State the blood parasite species.
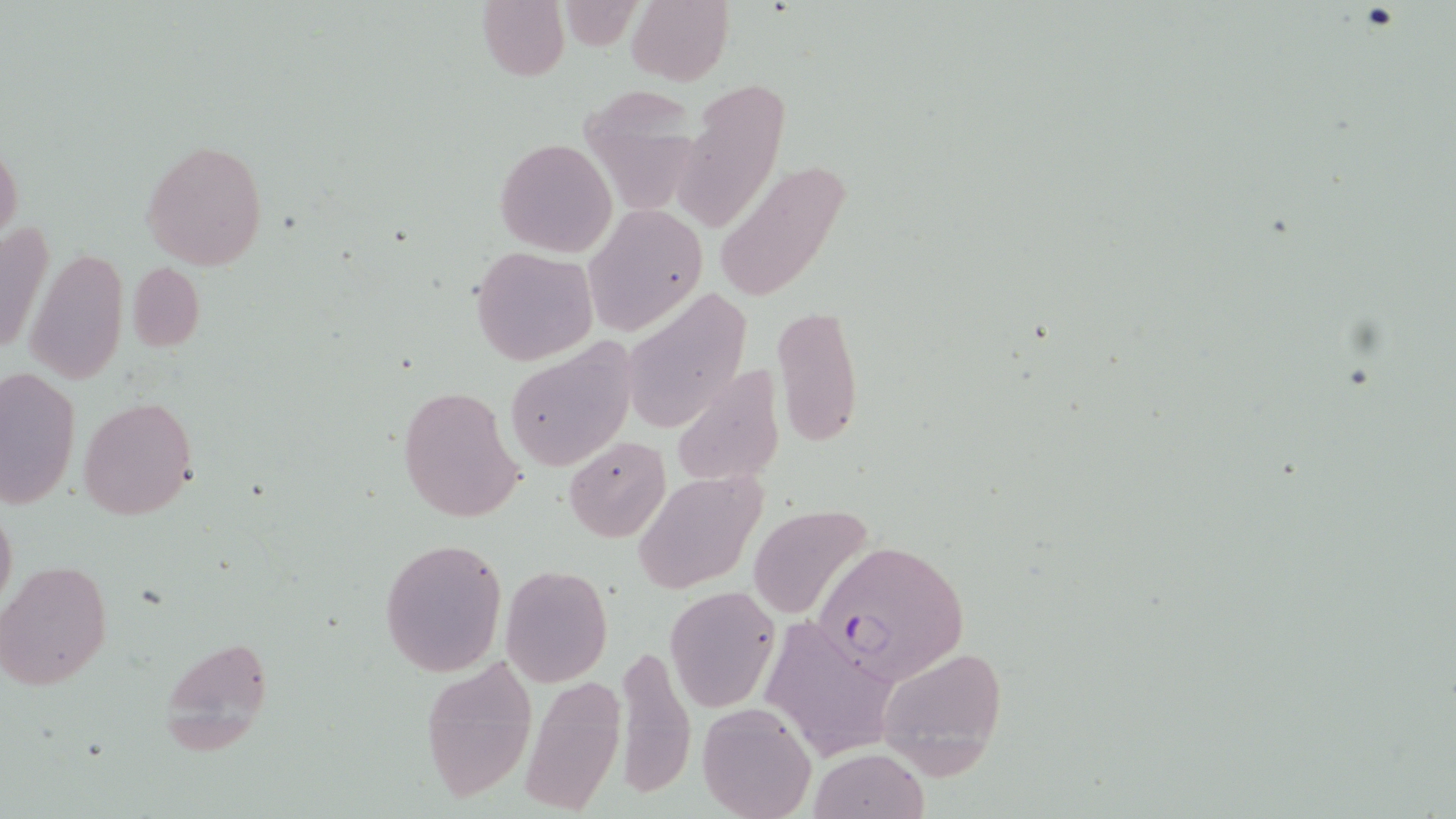

Plasmodium falciparum.

Summary:
  - Coordinate format: approximate bounding boxes as (x1, y1, x2, y2) in pixels
  - Uninfected red blood cell locations: (477, 0, 569, 81), (627, 0, 733, 86), (676, 78, 790, 229), (579, 87, 701, 222), (141, 138, 269, 271), (495, 138, 617, 257), (0, 141, 23, 249), (714, 159, 852, 304), (584, 205, 706, 337), (0, 219, 53, 363), (469, 246, 597, 366), (25, 247, 129, 385), (128, 262, 205, 352), (621, 292, 750, 435), (772, 304, 863, 448), (506, 344, 636, 472), (670, 365, 787, 490), (0, 366, 81, 511), (397, 385, 524, 522), (78, 397, 197, 520), (562, 435, 670, 542), (631, 469, 768, 594), (1, 501, 17, 613), (747, 505, 873, 620), (378, 537, 506, 676), (2, 561, 112, 689), (500, 564, 614, 686), (663, 586, 778, 712), (759, 613, 897, 767), (160, 634, 273, 751), (612, 642, 697, 800), (873, 642, 1008, 777), (420, 654, 539, 806), (521, 676, 625, 813), (697, 701, 816, 819), (806, 749, 928, 819)
  - Plasmodium falciparum-infected red blood cell locations: (813, 539, 969, 685)
  - Preparation: thin blood film
  - Magnification: 1000x
  - Stain: May-Grünwald-Giemsa
  - Field of view: one of a larger specimen
  - Modality: light microscopy
  - Image size: 1456×819 pixels